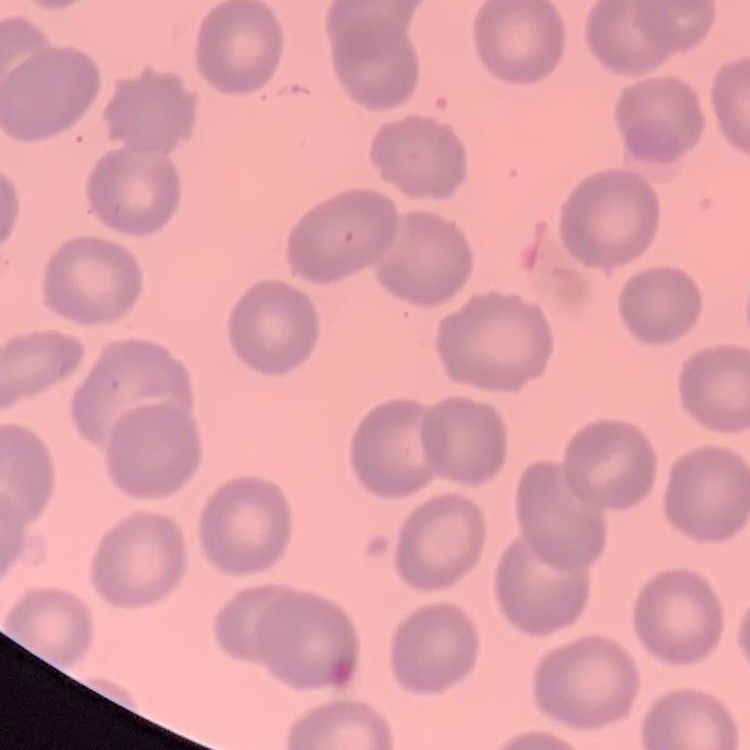 The erythrocytes exhibit no rouleaux formation. Thin peripheral smear. Square crop of a larger photomicrograph. Stained with either Field's or Giemsa.